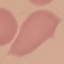 Result: no malaria parasites detected. Thin blood film. Giemsa-stained preparation. Photographed with a smartphone camera at the microscope eyepiece. Automatically extracted cell patch, resized to 64 × 64 pixels.